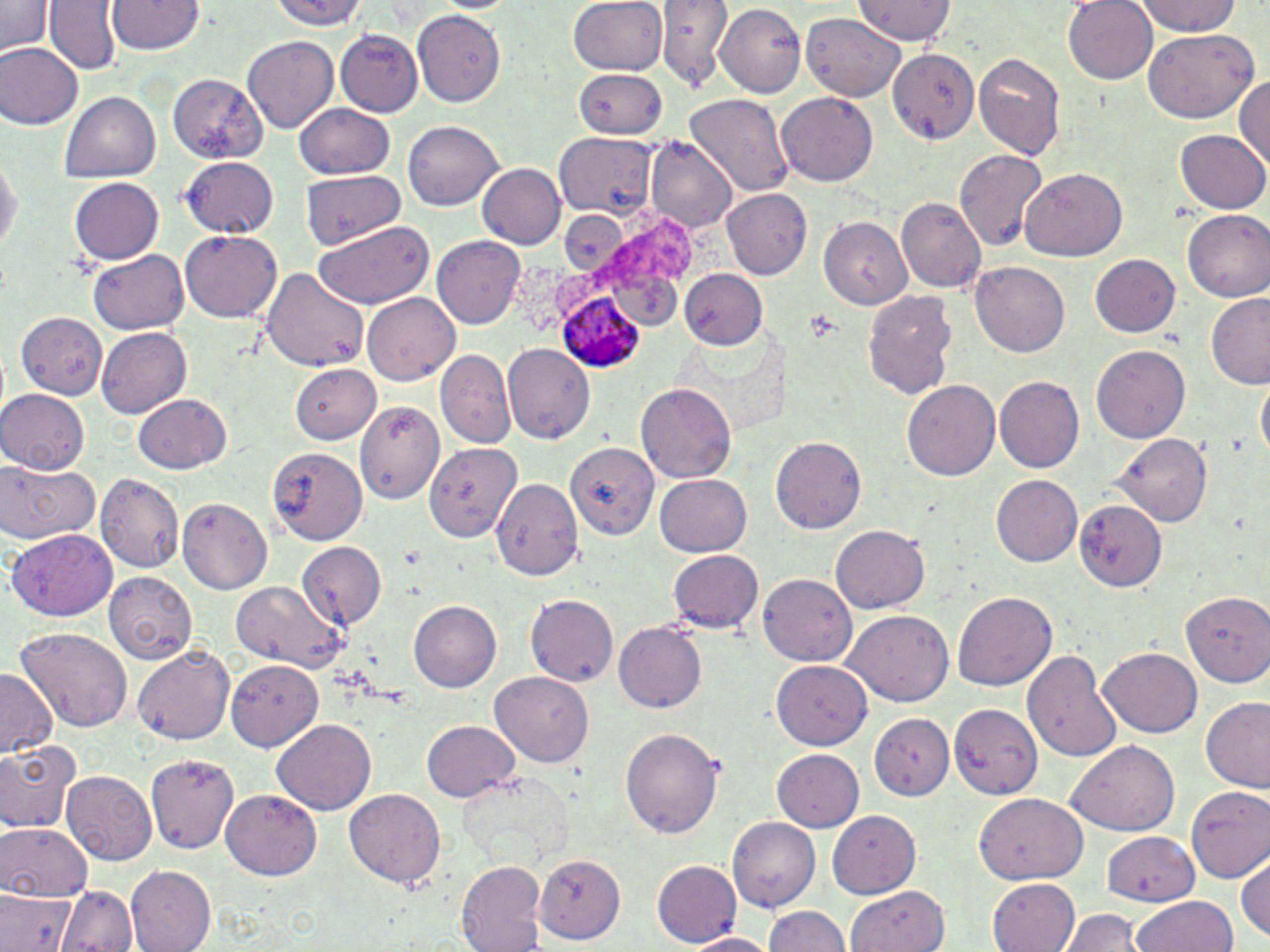
Summary:
  - Coordinate format: approximate bounding boxes as (x1,y1)-(x2,y2) corner pairs in pixels
  - Plasmodium ovale-infected red blood cell locations: (557,292)-(645,370)
  - Uninfected red blood cell locations: (46,0)-(121,75), (109,0)-(206,57), (267,0)-(369,31), (567,0)-(669,75), (658,0)-(732,88), (1064,0)-(1160,82), (1135,0)-(1244,38), (1,1)-(51,60), (854,1)-(958,47), (713,2)-(806,96), (412,11)-(506,106), (802,11)-(905,101), (335,30)-(422,115), (1143,32)-(1258,122), (244,35)-(338,133), (1,44)-(82,130), (886,46)-(982,149), (973,50)-(1067,159), (573,68)-(668,139), (1234,72)-(1270,175), (165,75)-(267,164), (60,91)-(162,184), (683,91)-(791,198), (776,93)-(879,186), (294,102)-(392,179), (404,120)-(502,212), (1177,130)-(1270,215), (553,133)-(658,215), (645,135)-(738,234), (956,149)-(1048,251), (0,152)-(20,262), (181,158)-(277,238), (476,164)-(563,250), (1018,168)-(1126,262), (299,171)-(405,250), (72,176)-(163,263), (721,189)-(814,280), (896,198)-(986,293), (1183,210)-(1270,301), (820,216)-(913,307), (314,222)-(433,310), (181,230)-(281,323), (433,237)-(527,329), (89,249)-(190,335), (1088,254)-(1181,339), (971,261)-(1069,357), (261,264)-(369,373), (681,268)-(768,351), (862,290)-(956,400), (363,293)-(461,386), (1207,293)-(1270,390), (17,311)-(110,398), (96,326)-(189,419), (503,344)-(593,444), (1090,346)-(1191,444), (436,350)-(513,447), (291,367)-(383,442), (994,376)-(1085,475), (1255,376)-(1268,464), (902,379)-(1001,482), (636,384)-(738,483), (0,389)-(90,476), (132,393)-(232,473), (359,400)-(445,503), (1114,434)-(1214,530), (771,436)-(866,535), (563,439)-(658,540), (425,442)-(522,546), (269,447)-(366,545), (0,456)-(102,548), (97,474)-(183,572), (654,474)-(752,557), (991,475)-(1083,567), (492,476)-(582,579), (178,498)-(272,595), (1070,501)-(1168,599), (832,523)-(929,611), (8,528)-(117,621), (295,541)-(386,629), (668,550)-(763,634), (105,571)-(197,659), (759,577)-(856,666), (229,582)-(347,673), (1181,589)-(1270,690), (953,592)-(1057,689), (528,594)-(621,686), (407,601)-(500,692), (843,609)-(954,705), (613,620)-(707,711), (14,627)-(131,737), (132,645)-(235,747), (1098,647)-(1201,736), (1024,650)-(1119,765), (227,661)-(325,750), (772,661)-(870,750), (0,669)-(58,756), (489,672)-(594,768), (1199,693)-(1270,795), (944,702)-(1040,799), (865,708)-(954,803), (272,718)-(376,815), (422,719)-(519,803), (620,727)-(724,838), (0,737)-(84,836), (1066,740)-(1179,839), (771,748)-(865,831), (149,754)-(241,855), (63,771)-(159,865), (456,773)-(575,870), (1185,785)-(1270,881), (223,789)-(324,879), (345,790)-(444,886), (973,793)-(1088,882), (829,806)-(922,900), (728,817)-(819,914), (0,819)-(93,901), (1101,830)-(1198,905), (1235,851)-(1270,942), (533,855)-(625,943), (652,860)-(740,946), (455,861)-(546,952), (125,867)-(216,952), (987,877)-(1080,952), (58,885)-(136,952), (850,886)-(946,952), (0,892)-(77,952), (1131,895)-(1238,952), (764,906)-(851,952), (1066,909)-(1140,952), (685,930)-(778,951)
  - Slide-level diagnosis: Plasmodium ovale
  - Image size: 1270×952 pixels
  - Field of view: one of a larger specimen
  - Modality: light microscopy
  - Preparation: thin blood film
  - Magnification: 1000x
  - Stain: May-Grünwald-Giemsa